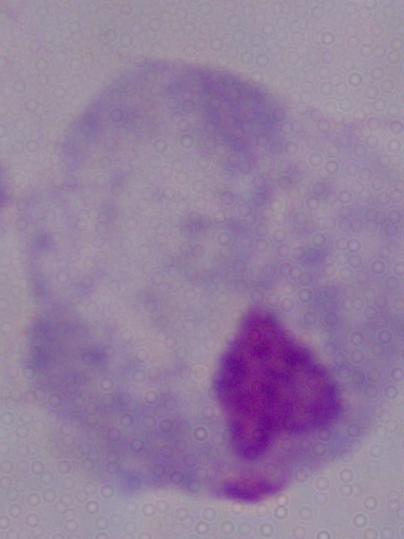

{
  "modality": "micrograph",
  "identification": "trichomonad",
  "magnification": "1000x"
}